Locate every P. falciparum parasite and identify its life-cycle stage.
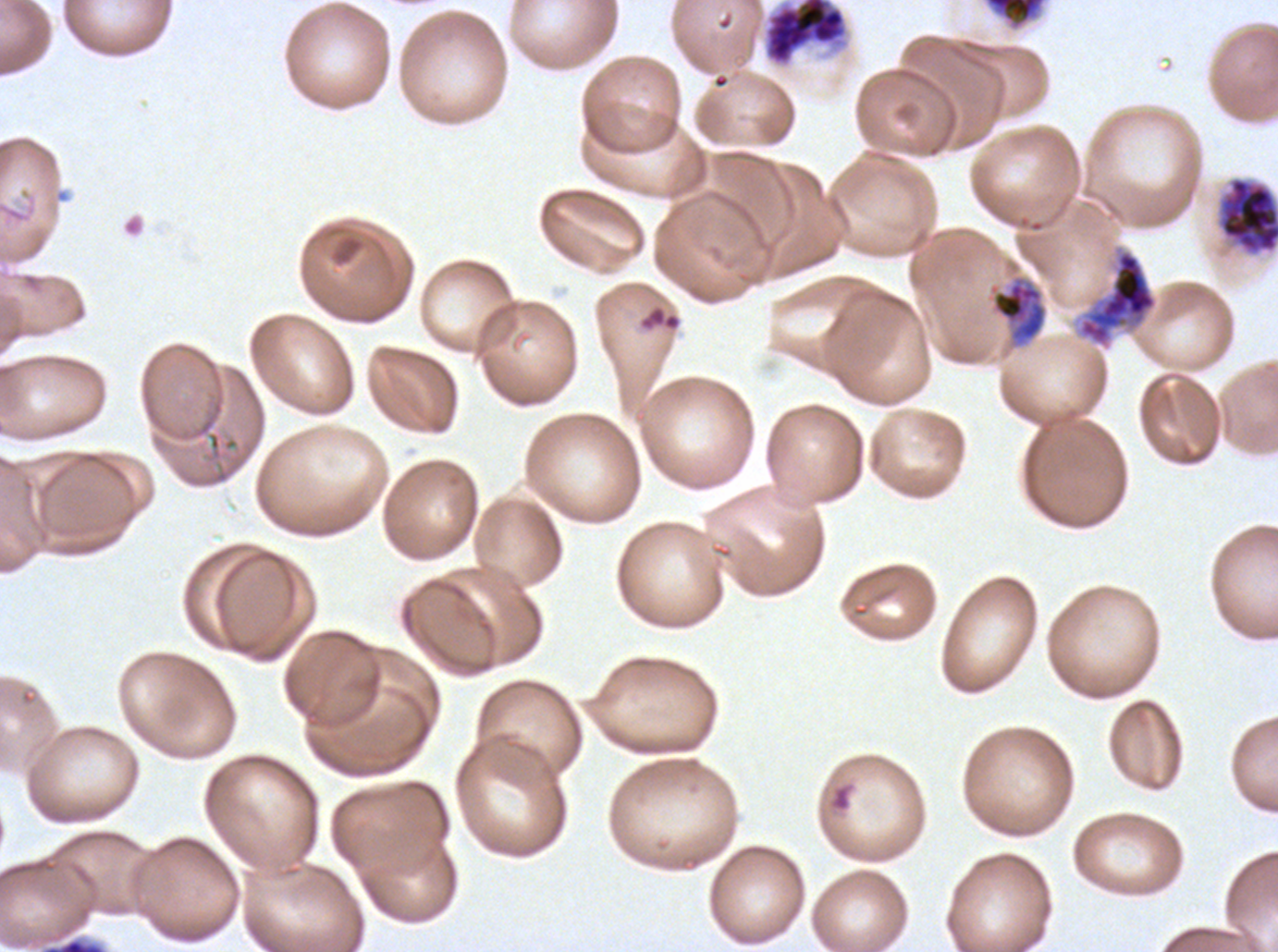

Approximate bounding boxes as {x1, y1, x2, y2} in pixels.
Rings: {828, 783, 852, 812}.
Mid trophozoites: {989, 275, 1047, 347}.
Early schizonts: {1076, 249, 1159, 348}.
Late schizonts: {761, 0, 851, 70}, {1217, 177, 1277, 256}.
Gametocytes: {983, 0, 1047, 31}.
No late-ring/early-trophozoite forms, late trophozoites, or segmenters observed.

debris locations = {6, 207, 25, 222}, {638, 305, 682, 332}
field of view = sub-image separated from a larger composite
preparation = thin blood film
life-cycle stages observed = ring, mid trophozoite, early schizont, late schizont, gametocyte
image size = 1278×952 pixels
stain = Giemsa
specimen = ex-vivo P. falciparum culture from a patient in The Gambia, grown for 24 to 48 hours